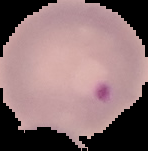

image type = cell region segmented out of the field of view; surrounding area masked to black
preparation = thin blood smear
malaria status = parasitized
image size = 148×151 pixels